Report the malaria status of this cell.
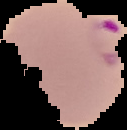

Parasitized.

image size = 127×130 pixels
preparation = thin blood film
image type = segmented cell region on a black background